Identify the parasite.
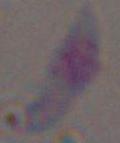

Toxoplasma gondii.

Summary:
  - Magnification: 1000x
  - Modality: micrograph